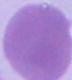

Captured at 1000x magnification. A red blood cell is shown. Micrograph.